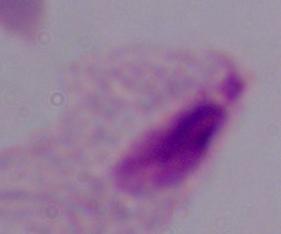
{
  "magnification": "1000x",
  "modality": "micrograph",
  "identification": "trichomonad"
}